Classify this cell by malaria status.
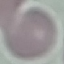

It is uninfected.

Cell patch, automatically extracted from a larger field of view and resized to 64 × 64 pixels. Giemsa-stained preparation. Photographed with a smartphone camera at the microscope eyepiece. Thin smear of blood.